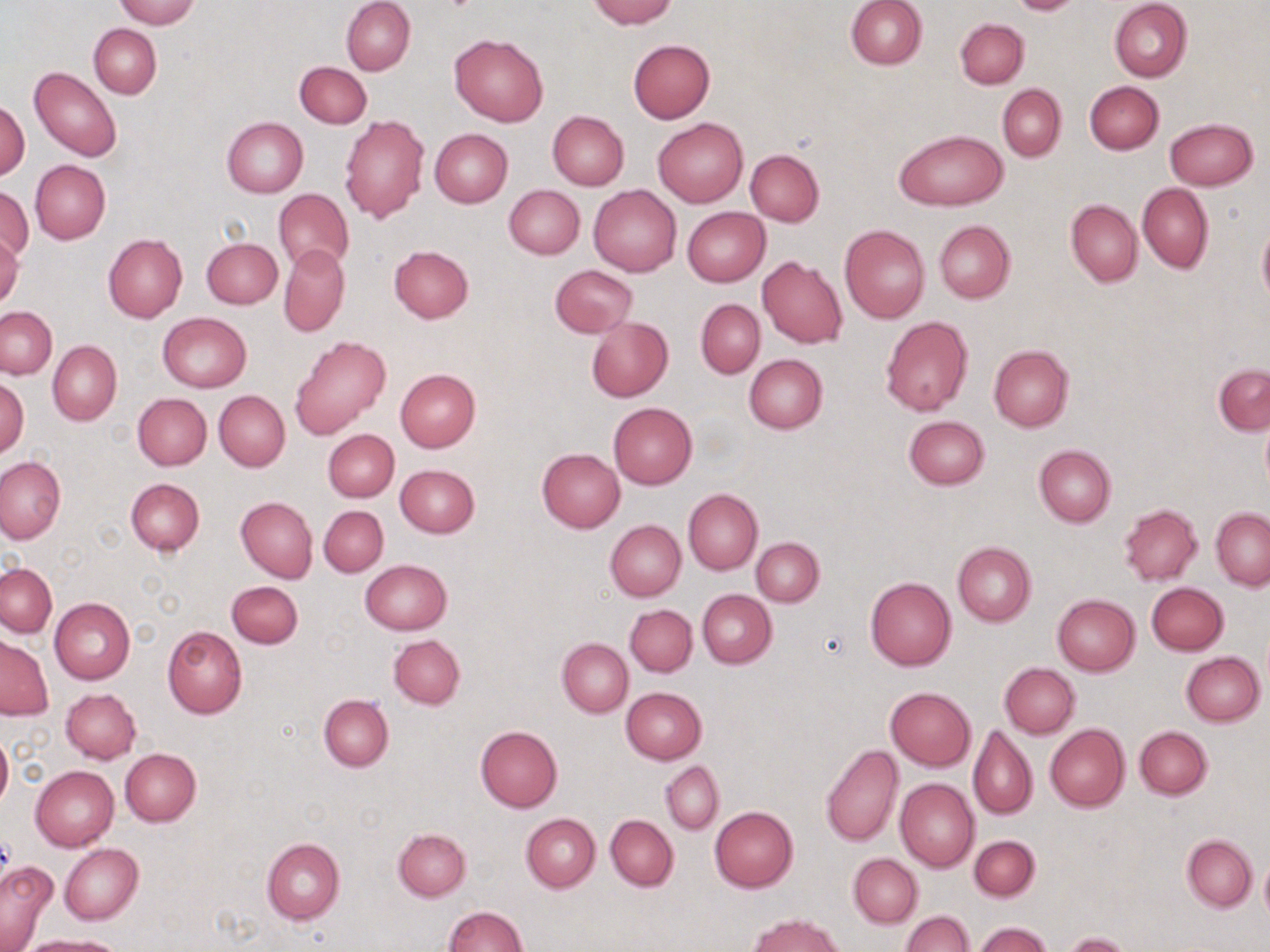

Summary:
  - Coordinate format: approximate bounding boxes as (x1, y1, x2, y2) in pixels
  - Uninfected red blood cell locations: (114, 0, 199, 27), (342, 0, 415, 76), (588, 0, 676, 28), (845, 0, 927, 70), (1010, 0, 1081, 15), (1109, 1, 1192, 82), (955, 18, 1029, 89), (89, 24, 160, 97), (450, 34, 548, 128), (628, 39, 715, 122), (295, 61, 371, 127), (30, 67, 121, 162), (1083, 81, 1164, 154), (997, 84, 1066, 160), (0, 101, 30, 180), (548, 111, 629, 190), (339, 113, 430, 223), (221, 117, 307, 197), (654, 118, 747, 207), (1166, 118, 1258, 190), (430, 129, 513, 207), (895, 130, 1006, 212), (745, 149, 825, 225), (30, 160, 111, 244), (1138, 183, 1214, 274), (505, 184, 584, 259), (590, 185, 682, 276), (1, 187, 33, 264), (274, 189, 353, 272), (1066, 199, 1143, 286), (682, 207, 770, 287), (933, 219, 1015, 304), (1257, 223, 1270, 307), (840, 225, 931, 323), (0, 233, 23, 310), (103, 235, 188, 322), (201, 238, 283, 309), (279, 244, 350, 337), (389, 245, 474, 322), (757, 257, 847, 349), (550, 264, 638, 338), (696, 299, 765, 377), (1, 307, 56, 379), (159, 312, 251, 391), (880, 316, 973, 417), (587, 317, 673, 402), (290, 336, 391, 439), (48, 340, 122, 425), (989, 345, 1074, 432), (744, 354, 828, 434), (1213, 364, 1270, 436), (394, 368, 481, 451), (0, 378, 29, 459), (215, 391, 288, 471), (133, 393, 211, 470), (608, 402, 697, 488), (903, 415, 991, 490), (323, 429, 399, 502), (1034, 444, 1116, 527), (537, 448, 625, 532), (0, 456, 67, 545), (395, 464, 480, 538), (126, 478, 204, 556), (683, 489, 762, 574), (235, 496, 317, 583), (1119, 504, 1203, 584), (319, 505, 388, 576), (1211, 508, 1269, 589), (605, 519, 686, 601), (752, 537, 824, 607), (952, 541, 1037, 626), (360, 559, 453, 635), (1, 563, 56, 636), (865, 577, 955, 670), (227, 581, 304, 649), (1146, 582, 1229, 655), (697, 590, 776, 668), (1052, 594, 1140, 674), (50, 597, 134, 684), (625, 604, 697, 676), (162, 626, 246, 719), (388, 634, 465, 709), (1, 636, 53, 720), (557, 638, 633, 717), (1181, 652, 1264, 726), (999, 663, 1080, 739), (620, 687, 706, 764), (885, 687, 976, 770), (60, 688, 141, 763), (319, 694, 393, 772), (967, 723, 1038, 819), (1045, 723, 1129, 811), (475, 726, 563, 812), (1134, 726, 1211, 799), (0, 731, 12, 813), (820, 744, 902, 848), (120, 749, 201, 826), (661, 761, 724, 834), (30, 765, 119, 852), (895, 778, 979, 871), (709, 806, 799, 892), (520, 813, 600, 892), (605, 815, 678, 891), (393, 827, 471, 900), (968, 835, 1040, 902), (1181, 835, 1257, 911), (262, 839, 345, 924), (59, 844, 143, 925), (848, 853, 922, 928), (1259, 855, 1270, 923), (0, 858, 58, 951), (443, 906, 527, 951), (900, 912, 974, 952), (748, 914, 844, 952), (976, 922, 1052, 952), (1063, 933, 1134, 952), (17, 935, 124, 951)
  - Slide-level diagnosis: no evidence of blood parasites
  - Field of view: one of a larger specimen
  - Modality: optical microscopy
  - Image size: 1270×952 pixels
  - Preparation: thin blood smear
  - Magnification: 1000x
  - Stain: May-Grünwald-Giemsa